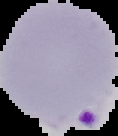

Summary:
  - Image type: segmented cell region on a black background
  - Image size: 118×136 pixels
  - Preparation: thin blood smear
  - Malaria status: parasitized